Assess the morphology of the red blood cells.
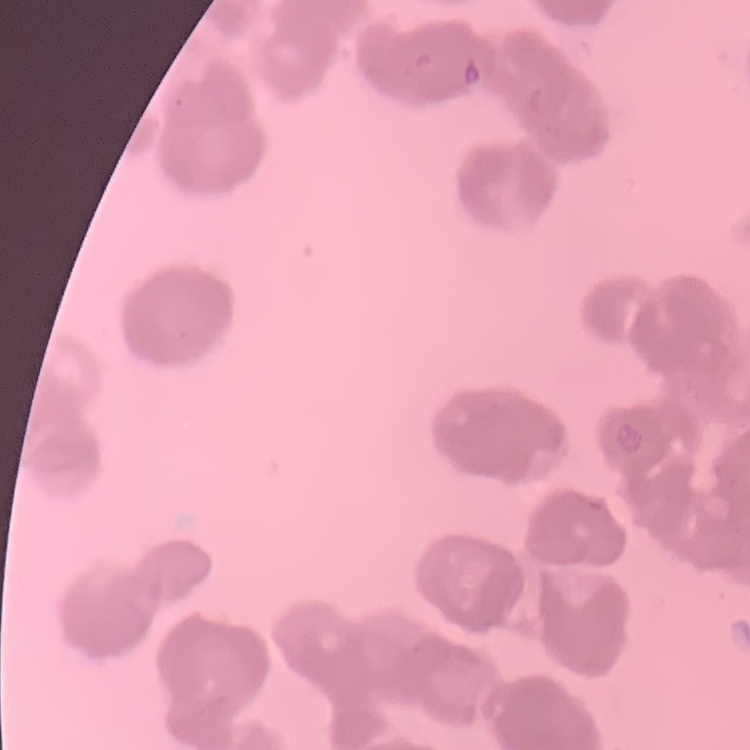
They show rouleaux formation.

image type = one tile cut from a larger photomicrograph
preparation = thin peripheral smear
stain = Field's or Giemsa